Identify the cell.
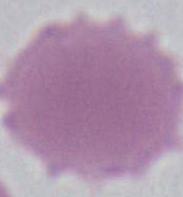
This is an erythrocyte.

Summary:
  - Magnification: 1000x
  - Modality: micrograph